Classify this cell by malaria status.
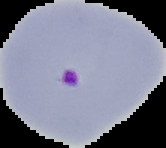

Parasitized.

Summary:
  - Image size: 166×148 pixels
  - Image type: segmented cell region with the area outside set to black
  - Preparation: thin blood film